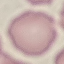

malaria status = uninfected
capture = smartphone camera at the microscope eyepiece
stain = Giemsa
image type = cell patch, automatically extracted from a larger field of view and resized to 64 × 64 pixels
preparation = thin blood film